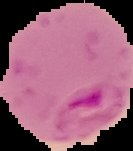
Summary:
  - Result: malaria parasites detected
  - Image type: segmented cell region on a black background
  - Image size: 133×151 pixels
  - Preparation: thin blood film